Outline each blood parasite and name the species.
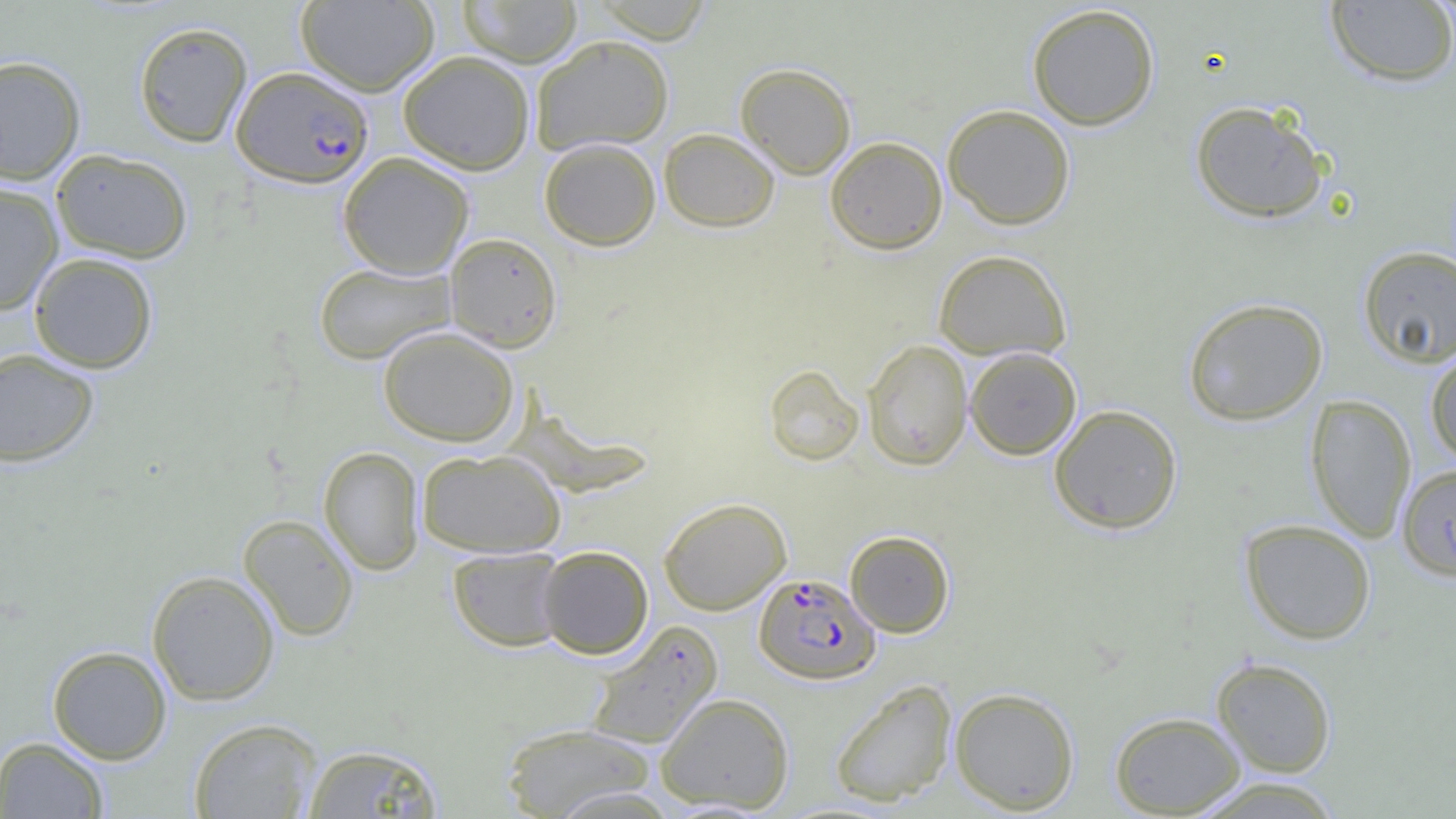
Approximate bounding boxes as (x1, y1, x2, y2) in pixels.
Plasmodium falciparum-infected red blood cells: (232, 66, 374, 188), (753, 573, 880, 684).
No Plasmodium ovale, Plasmodium malariae, Plasmodium vivax, Babesia divergens, or Trypanosoma brucei observed.

Uninfected red blood cell locations: (457, 0, 583, 67), (588, 0, 714, 43), (296, 1, 439, 96), (1325, 1, 1456, 87), (1026, 3, 1160, 130), (133, 21, 252, 148), (531, 35, 675, 155), (397, 50, 535, 175), (0, 55, 86, 185), (735, 62, 857, 179), (1189, 100, 1329, 223), (942, 104, 1076, 230), (658, 128, 780, 232), (825, 136, 948, 254), (538, 138, 661, 251), (51, 148, 193, 263), (337, 152, 474, 279), (0, 182, 64, 316), (444, 233, 562, 352), (1357, 246, 1456, 368), (933, 249, 1072, 361), (29, 252, 158, 373), (313, 262, 457, 365), (1183, 296, 1328, 426), (378, 326, 519, 447), (862, 338, 973, 471), (1425, 346, 1456, 467), (965, 347, 1081, 459), (0, 348, 100, 468), (763, 363, 864, 465), (1305, 393, 1417, 543), (1048, 404, 1183, 534), (318, 446, 424, 576), (416, 448, 566, 558), (1399, 467, 1456, 585), (658, 497, 791, 615), (238, 513, 359, 641), (1239, 519, 1376, 645), (845, 530, 955, 637), (537, 545, 654, 659), (447, 546, 567, 651), (146, 570, 280, 706), (586, 620, 723, 749), (47, 645, 172, 764), (1211, 657, 1337, 777), (830, 679, 957, 808), (949, 686, 1080, 815), (656, 692, 794, 813), (1109, 710, 1246, 817), (188, 717, 324, 819), (499, 722, 657, 818), (0, 736, 109, 818), (302, 743, 446, 818), (1188, 776, 1347, 819), (548, 787, 681, 819). Slide-level diagnosis: Plasmodium falciparum. 1000x magnification. One field of a larger specimen. Image is 1456×819 pixels. Optical microscopy. Thin blood film.